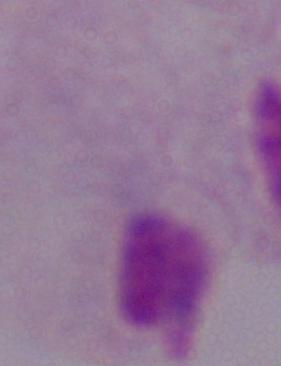
Photomicrograph. Captured at 1000x magnification. A trichomonad is shown.